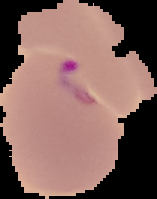

{
  "malaria_status": "parasitized",
  "image_size": "157×199 pixels",
  "preparation": "thin blood smear",
  "image_type": "cell region segmented out of the field of view; surrounding area masked to black"
}